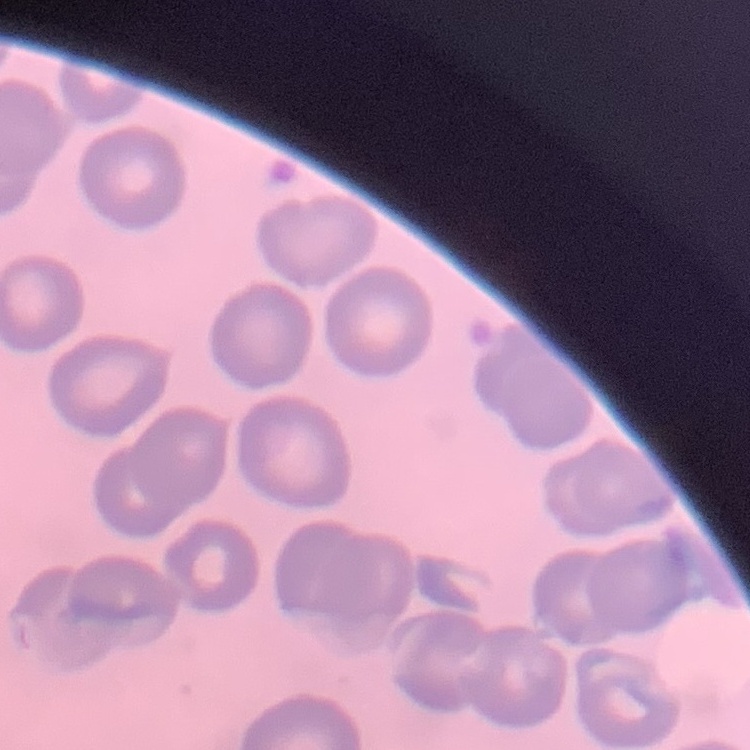
Summary:
  - Erythrocyte morphology: no rouleaux formation
  - Preparation: thin blood smear
  - Image type: one tile cut from a larger photomicrograph
  - Stain: Field's or Giemsa